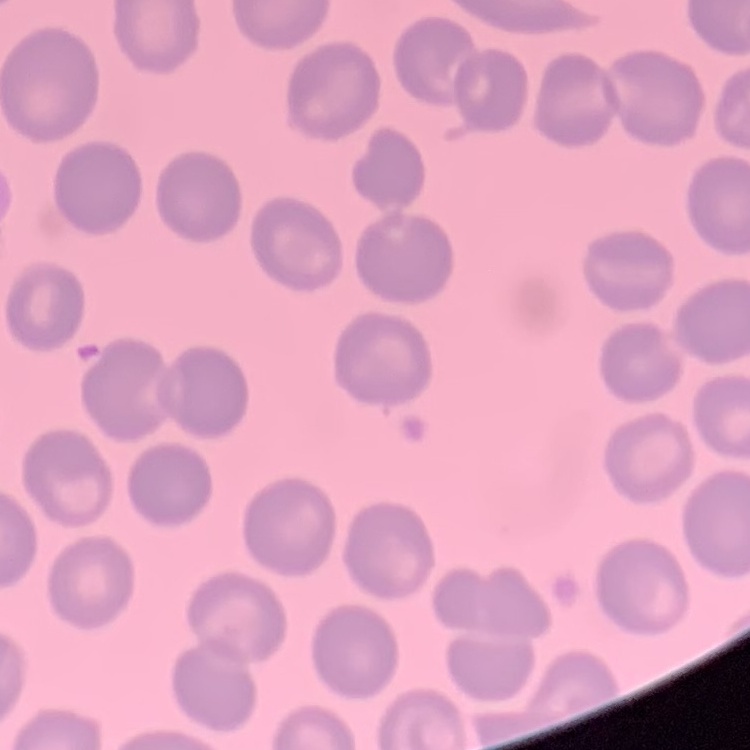
Summary:
  - Erythrocyte morphology: no rouleaux formation
  - Preparation: thin blood smear
  - Stain: Field's or Giemsa
  - Image type: square crop of a larger photomicrograph